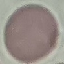
Result: negative for malaria parasites. Photographed with a smartphone camera at the microscope eyepiece. Thin smear of blood. Automatically extracted cell patch, resized to 64 × 64 pixels. Giemsa-stained preparation.